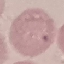

result = no malaria parasites seen
preparation = thin smear
capture = smartphone camera at the microscope eyepiece
stain = Giemsa
image type = cell patch, automatically extracted from a larger field of view and resized to 64 × 64 pixels